Classify this cell by malaria status.
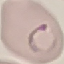

It is parasitized.

Summary:
  - Preparation: thin smear
  - Capture: smartphone through the microscope eyepiece
  - Image type: automatically extracted cell patch, resized to 64 × 64 pixels
  - Stain: Giemsa